Give the extent of all Plasmodium vivax-infected red blood cells.
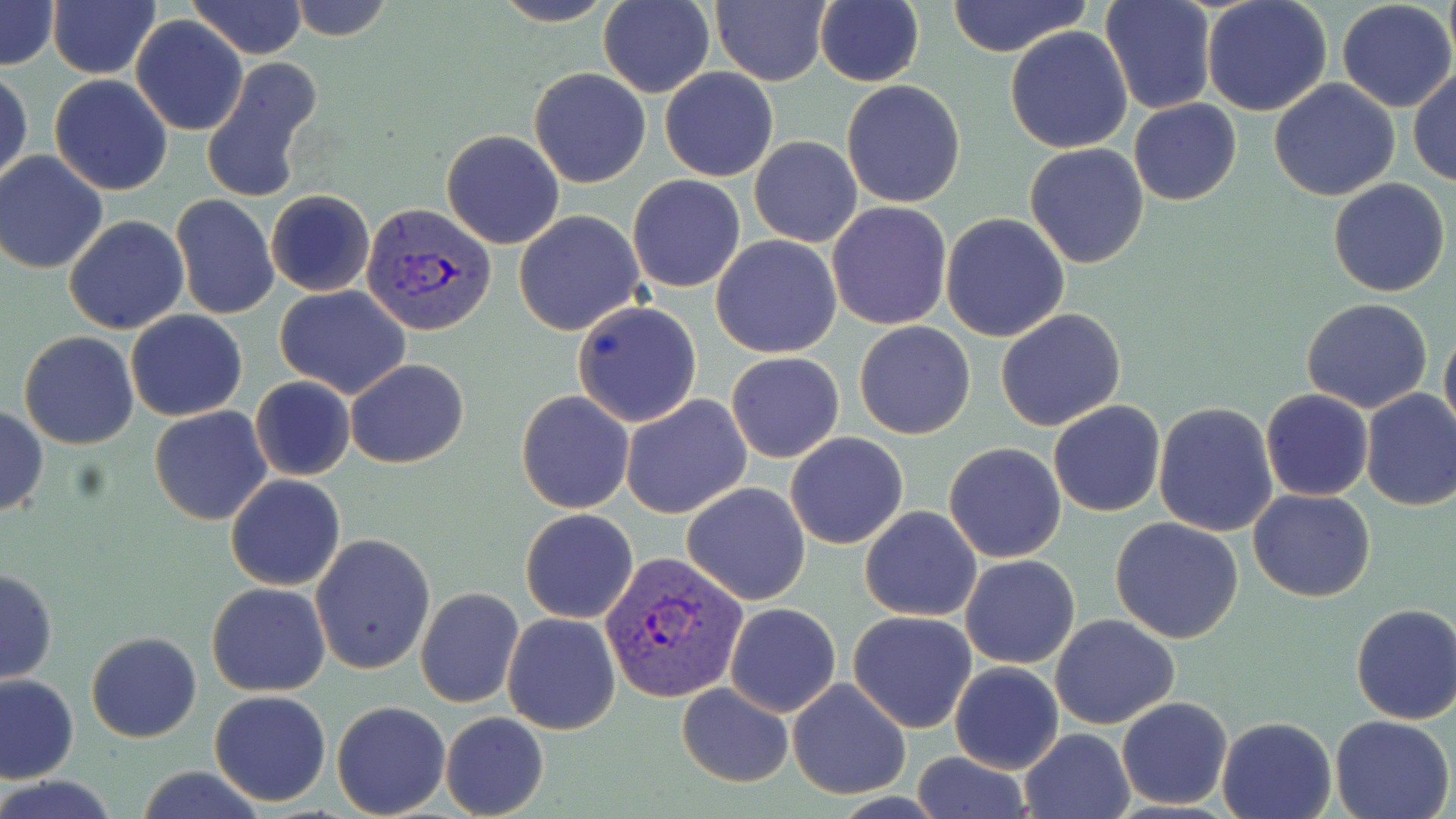

Approximate bounding boxes as (x1,y1)-(x2,y2) corner pairs in pixels.
Plasmodium vivax-infected red blood cells: (360,200)-(497,338), (601,553)-(749,704).

Summary:
  - Uninfected red blood cell locations: (0,0)-(59,70), (46,0)-(161,79), (187,0)-(309,61), (285,0)-(394,41), (489,0)-(617,27), (598,0)-(714,98), (711,0)-(833,87), (814,0)-(925,88), (1101,0)-(1215,116), (1201,0)-(1333,118), (944,1)-(1091,57), (1335,1)-(1455,113), (132,15)-(248,135), (1005,25)-(1132,153), (200,56)-(324,204), (528,67)-(652,188), (660,67)-(778,181), (1408,68)-(1456,187), (1,69)-(33,188), (49,74)-(174,196), (1267,79)-(1401,202), (841,80)-(967,209), (1128,99)-(1242,206), (441,128)-(564,248), (749,137)-(862,247), (1024,142)-(1150,267), (0,151)-(109,274), (627,174)-(747,292), (1327,178)-(1452,297), (265,190)-(376,296), (171,193)-(279,320), (827,200)-(952,330), (514,210)-(645,337), (941,213)-(1071,341), (64,215)-(190,334), (710,235)-(842,358), (276,285)-(412,398), (1301,297)-(1434,414), (573,300)-(703,428), (995,307)-(1126,430), (125,310)-(249,422), (854,321)-(976,439), (1439,324)-(1456,442), (20,332)-(139,449), (726,352)-(845,463), (346,359)-(469,469), (249,376)-(356,482), (1360,388)-(1456,513), (1261,389)-(1374,501), (516,391)-(633,513), (620,394)-(751,520), (1047,400)-(1165,517), (1152,402)-(1278,539), (0,406)-(48,517), (149,406)-(273,527), (785,431)-(908,549), (943,442)-(1067,563), (225,474)-(346,590), (682,481)-(811,605), (1249,488)-(1376,603), (859,505)-(982,621), (519,508)-(638,623), (1110,517)-(1243,644), (310,533)-(436,675), (959,554)-(1080,670), (0,567)-(58,684), (207,581)-(330,695), (414,587)-(524,709), (722,602)-(842,717), (1349,603)-(1456,725), (848,610)-(978,732), (502,612)-(621,735), (1050,614)-(1180,728), (86,630)-(201,742), (949,661)-(1064,773), (0,673)-(78,785), (787,678)-(911,800), (676,682)-(795,788), (209,690)-(331,806), (1115,695)-(1234,808), (332,700)-(452,818), (440,712)-(549,819), (1329,713)-(1454,819), (1216,716)-(1337,819), (1020,728)-(1133,818), (910,752)-(1033,819), (134,765)-(268,819), (2,776)-(120,818)
  - Slide-level diagnosis: Plasmodium vivax
  - Modality: light microscopy
  - Field of view: single
  - Image size: 1456×819 pixels
  - Magnification: 1000x
  - Preparation: thin blood film
  - Stain: May-Grünwald-Giemsa